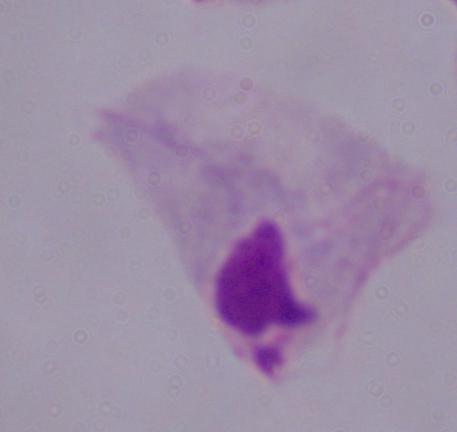 Captured at 1000x magnification. Photomicrograph. A trichomonad is seen.